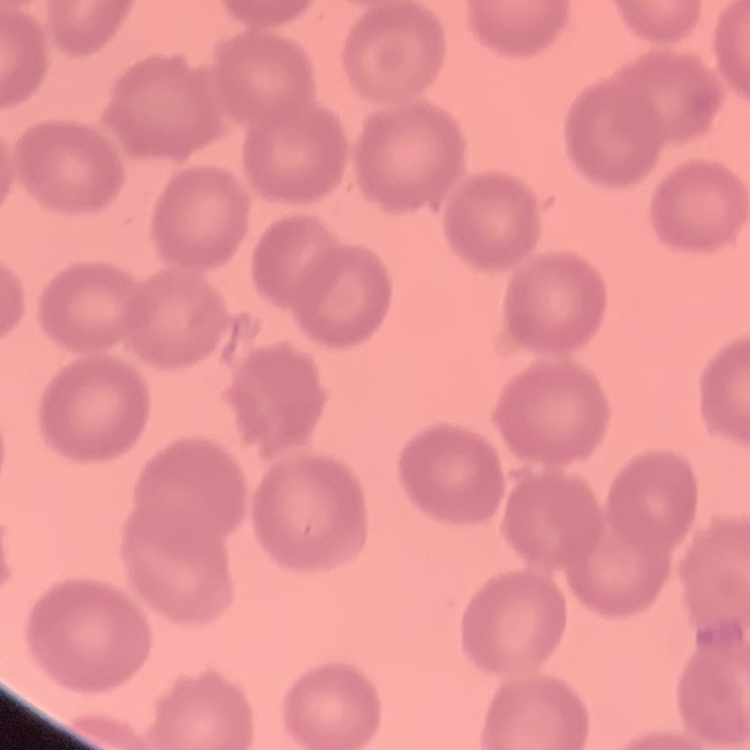

Summary:
  - Red blood cell morphology: no rouleaux formation
  - Preparation: thin blood film
  - Stain: Field's or Giemsa
  - Image type: square crop of a larger photomicrograph